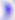

Summary:
  - Identification: Toxoplasma gondii
  - Magnification: 400x
  - Modality: micrograph